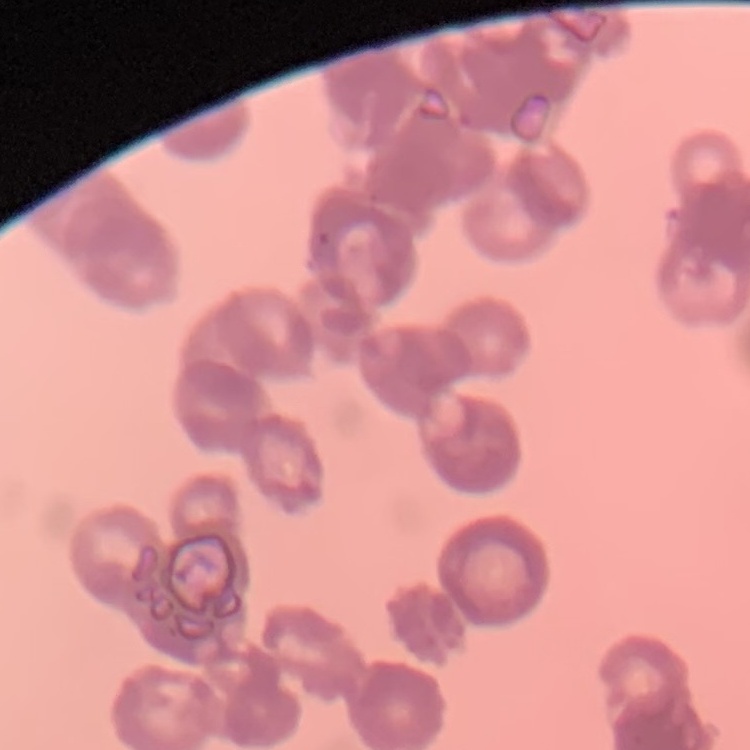

red blood cell morphology = rouleaux formation
image type = one tile cut from a larger photomicrograph
stain = Field's or Giemsa
preparation = thin blood smear